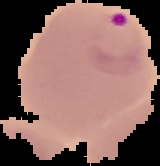
Summary:
  - Image type: segmented cell region on a black background
  - Malaria status: parasitized
  - Preparation: thin blood film
  - Image size: 160×166 pixels